Name the cell type shown.
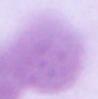

An erythrocyte.

1000x magnification. Micrograph.